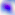

magnification = 400x
modality = micrograph
identification = Toxoplasma gondii